Describe the morphology of the erythrocytes.
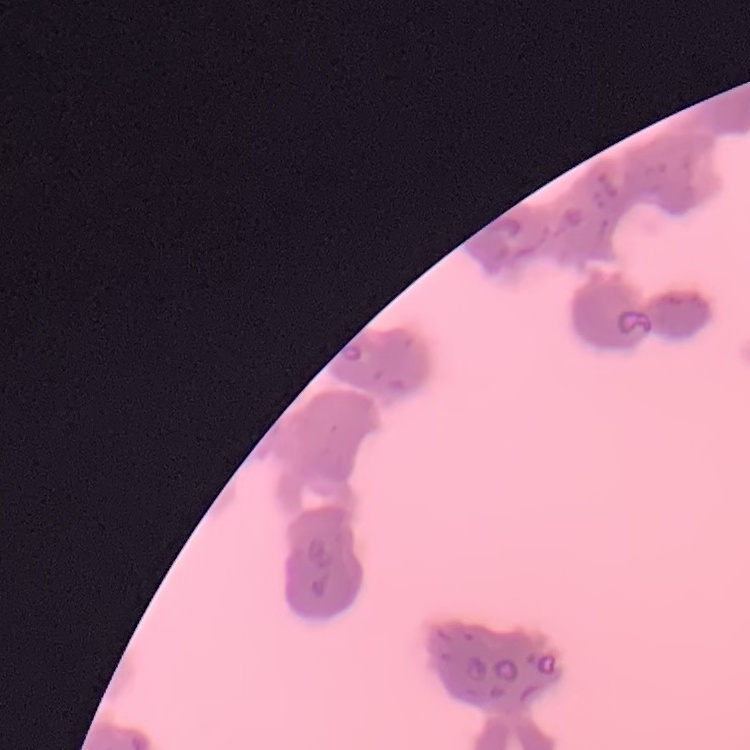
They show rouleaux formation.

Field's or Giemsa stain. Square crop of a larger photomicrograph. Thin peripheral smear.